Assess this cell for malaria.
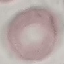

Uninfected.

stain = Giemsa
capture = smartphone camera at the microscope eyepiece
preparation = thin smear
image type = cell patch, automatically extracted from a larger field of view and resized to 64 × 64 pixels